Comment on the morphology of the erythrocytes.
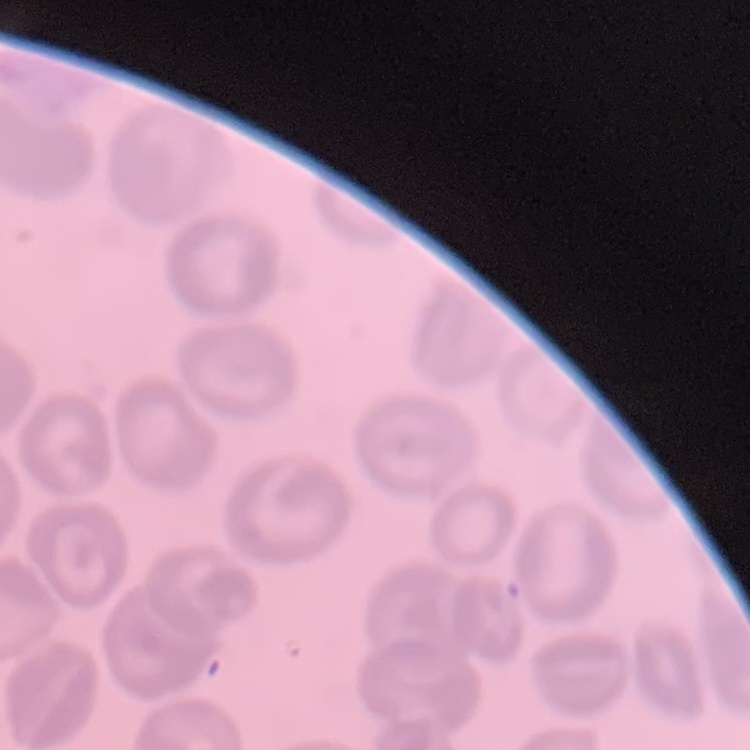
They show no rouleaux formation.

stain = Field's or Giemsa
image type = square crop of a larger photomicrograph
preparation = thin blood smear